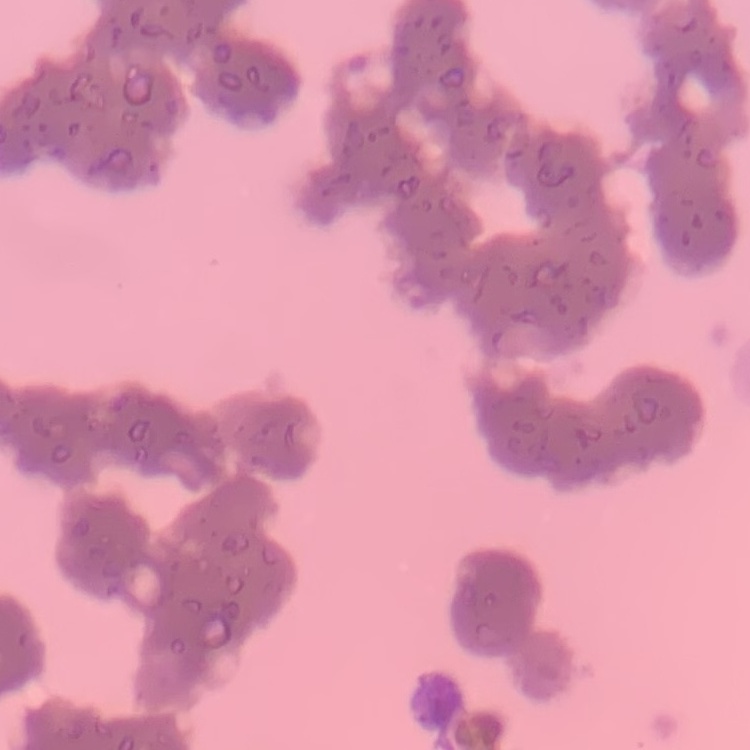
{
  "erythrocyte_morphology": "rouleaux formation",
  "preparation": "thin peripheral smear",
  "stain": "Field's or Giemsa",
  "image_type": "one tile cut from a larger photomicrograph"
}